Report the malaria status of this cell.
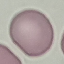
Uninfected.

preparation = thin blood film
stain = Giemsa
image type = automatically extracted cell patch, resized to 64 × 64 pixels
capture = smartphone through the microscope eyepiece